Outline each blood parasite and name the species.
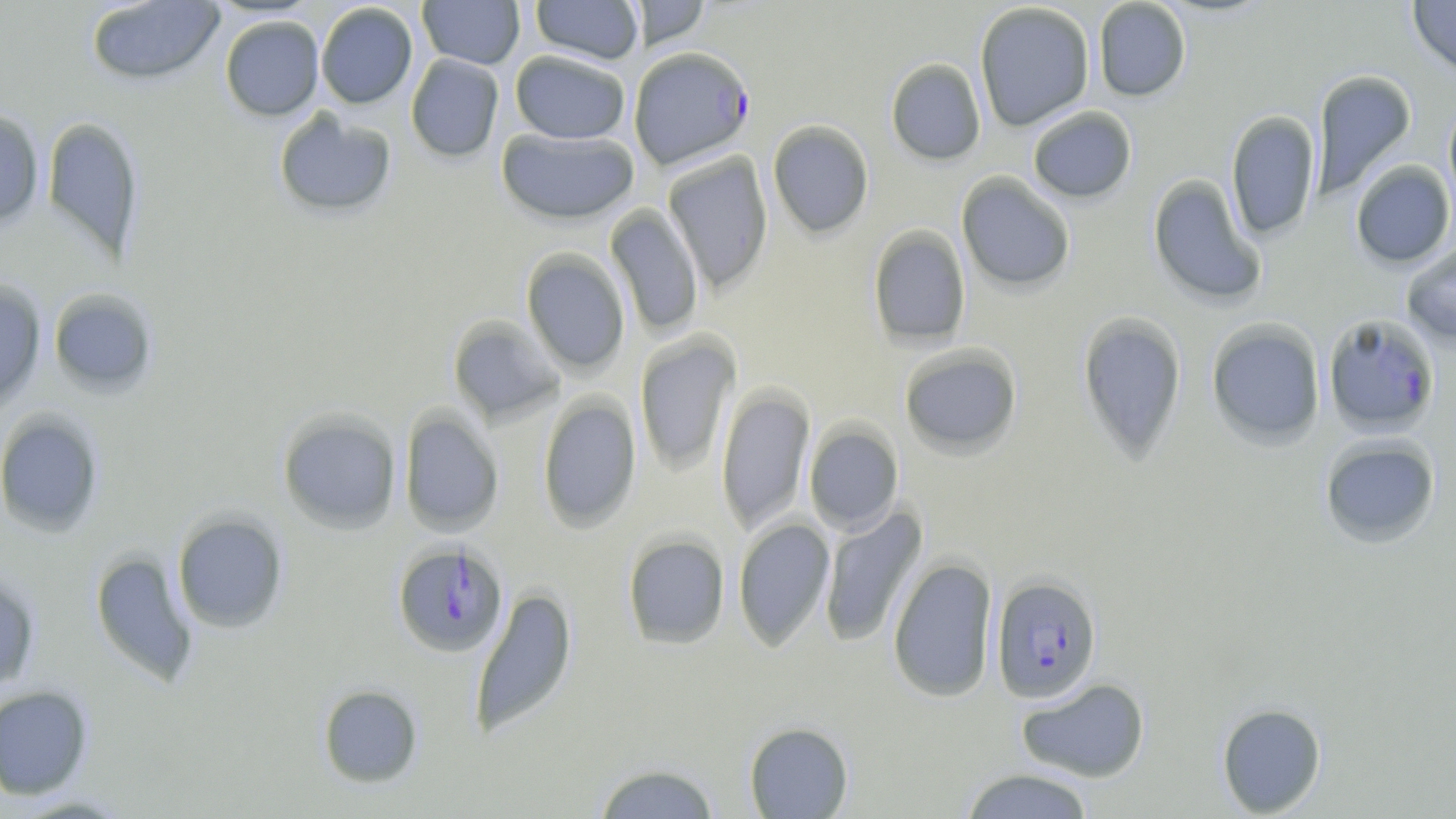
Approximate bounding boxes as named x1/y1/x2/y2 corners in pixels.
Plasmodium falciparum-infected red blood cells: (x1=629, y1=46, x2=755, y2=170), (x1=1322, y1=313, x2=1441, y2=436), (x1=392, y1=542, x2=509, y2=658), (x1=991, y1=575, x2=1102, y2=703).
No Plasmodium ovale, Plasmodium malariae, Plasmodium vivax, Babesia divergens, or Trypanosoma brucei observed.

slide-level diagnosis = Plasmodium falciparum
field of view = one of a larger specimen
magnification = 1000x
preparation = thin blood smear
stain = May-Grünwald-Giemsa
uninfected red blood cell locations = approximate bounding boxes as named x1/y1/x2/y2 corners in pixels: (x1=417, y1=0, x2=525, y2=69), (x1=530, y1=0, x2=644, y2=65), (x1=1093, y1=0, x2=1191, y2=101), (x1=1407, y1=0, x2=1456, y2=80), (x1=85, y1=1, x2=226, y2=86), (x1=629, y1=1, x2=711, y2=51), (x1=315, y1=2, x2=418, y2=109), (x1=974, y1=2, x2=1095, y2=131), (x1=219, y1=16, x2=324, y2=121), (x1=510, y1=50, x2=631, y2=144), (x1=405, y1=54, x2=504, y2=163), (x1=885, y1=58, x2=986, y2=165), (x1=1311, y1=70, x2=1417, y2=198), (x1=1443, y1=94, x2=1456, y2=215), (x1=1027, y1=106, x2=1137, y2=204), (x1=272, y1=108, x2=397, y2=219), (x1=0, y1=109, x2=45, y2=230), (x1=1225, y1=110, x2=1322, y2=241), (x1=42, y1=116, x2=145, y2=261), (x1=767, y1=120, x2=875, y2=239), (x1=495, y1=128, x2=639, y2=225), (x1=662, y1=151, x2=774, y2=294), (x1=1350, y1=160, x2=1456, y2=269), (x1=956, y1=172, x2=1076, y2=293), (x1=1147, y1=174, x2=1267, y2=307), (x1=605, y1=205, x2=704, y2=337), (x1=867, y1=225, x2=972, y2=349), (x1=1401, y1=241, x2=1456, y2=348), (x1=520, y1=248, x2=631, y2=375), (x1=0, y1=278, x2=47, y2=415), (x1=48, y1=288, x2=160, y2=397), (x1=1077, y1=312, x2=1187, y2=462), (x1=447, y1=315, x2=565, y2=427), (x1=1206, y1=319, x2=1326, y2=449), (x1=635, y1=333, x2=741, y2=474), (x1=899, y1=344, x2=1023, y2=458), (x1=716, y1=385, x2=815, y2=534), (x1=537, y1=394, x2=642, y2=532), (x1=277, y1=408, x2=402, y2=534), (x1=398, y1=408, x2=504, y2=537), (x1=0, y1=410, x2=105, y2=537), (x1=804, y1=422, x2=904, y2=534), (x1=1318, y1=435, x2=1441, y2=548), (x1=819, y1=505, x2=927, y2=649), (x1=172, y1=511, x2=289, y2=633), (x1=733, y1=517, x2=835, y2=651), (x1=622, y1=533, x2=730, y2=649), (x1=90, y1=550, x2=199, y2=686), (x1=887, y1=557, x2=998, y2=702), (x1=0, y1=568, x2=41, y2=692), (x1=469, y1=586, x2=578, y2=739), (x1=1016, y1=677, x2=1150, y2=783), (x1=317, y1=684, x2=423, y2=788), (x1=0, y1=685, x2=94, y2=799), (x1=1216, y1=702, x2=1327, y2=817), (x1=743, y1=722, x2=854, y2=818), (x1=592, y1=762, x2=721, y2=818), (x1=958, y1=767, x2=1096, y2=818), (x1=10, y1=793, x2=134, y2=817)
modality = light microscopy
image size = 1456×819 pixels